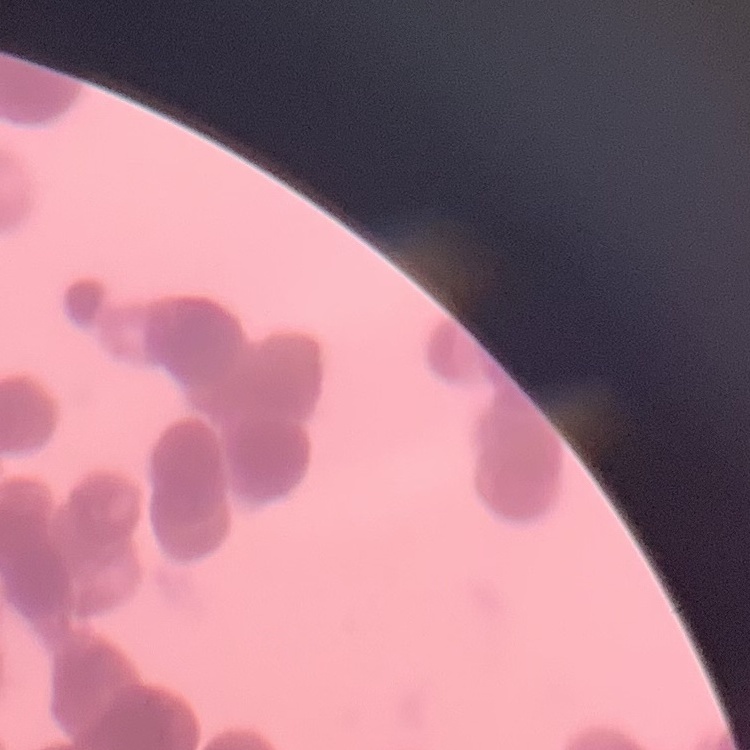
The erythrocytes show rouleaux formation. One tile cut from a larger photomicrograph. Stained with either Field's or Giemsa. Thin peripheral smear.